Point out each Plasmodium parasite.
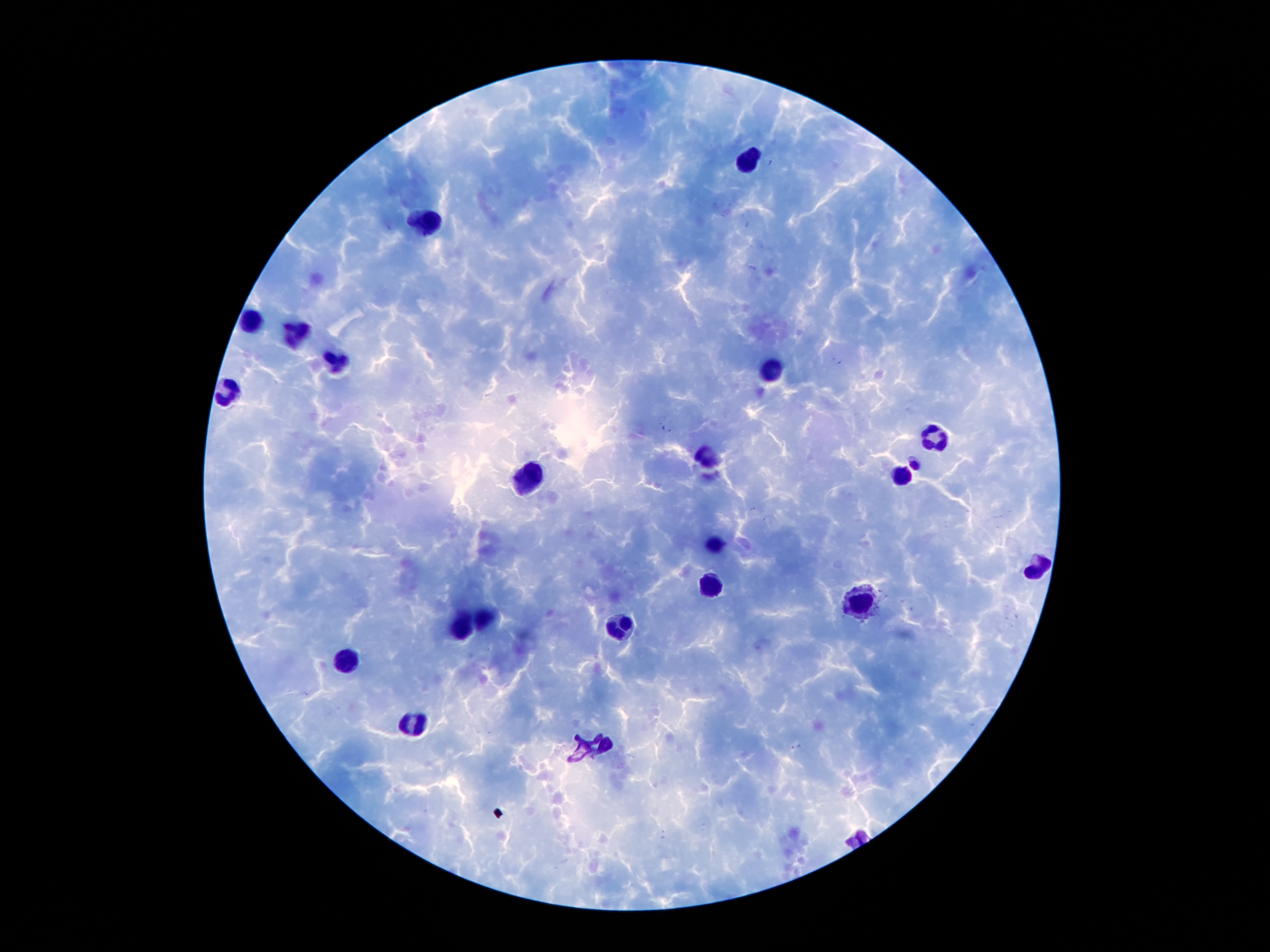

Approximate centers as [x, y] in pixels.
Plasmodium parasites: [915, 462].

Summary:
  - Leukocyte locations: [749, 157], [431, 219], [257, 321], [293, 330], [338, 362], [770, 375], [227, 389], [938, 434], [709, 455], [529, 473], [904, 475], [718, 543], [1038, 564], [713, 582], [861, 602], [486, 614], [466, 625], [618, 627], [352, 659], [416, 720]
  - Capture: smartphone through the microscope eyepiece
  - Stain: Giemsa
  - Field of view: one from this slide
  - Preparation: thick blood film
  - Patient malaria status: positive for Plasmodium falciparum
  - Image size: 1270×952 pixels
  - Magnification: 100x